Identify the parasite.
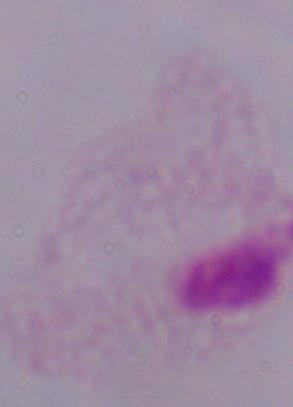
A trichomonad.

modality = photomicrograph
magnification = 1000x